Outline each blood parasite and name the species.
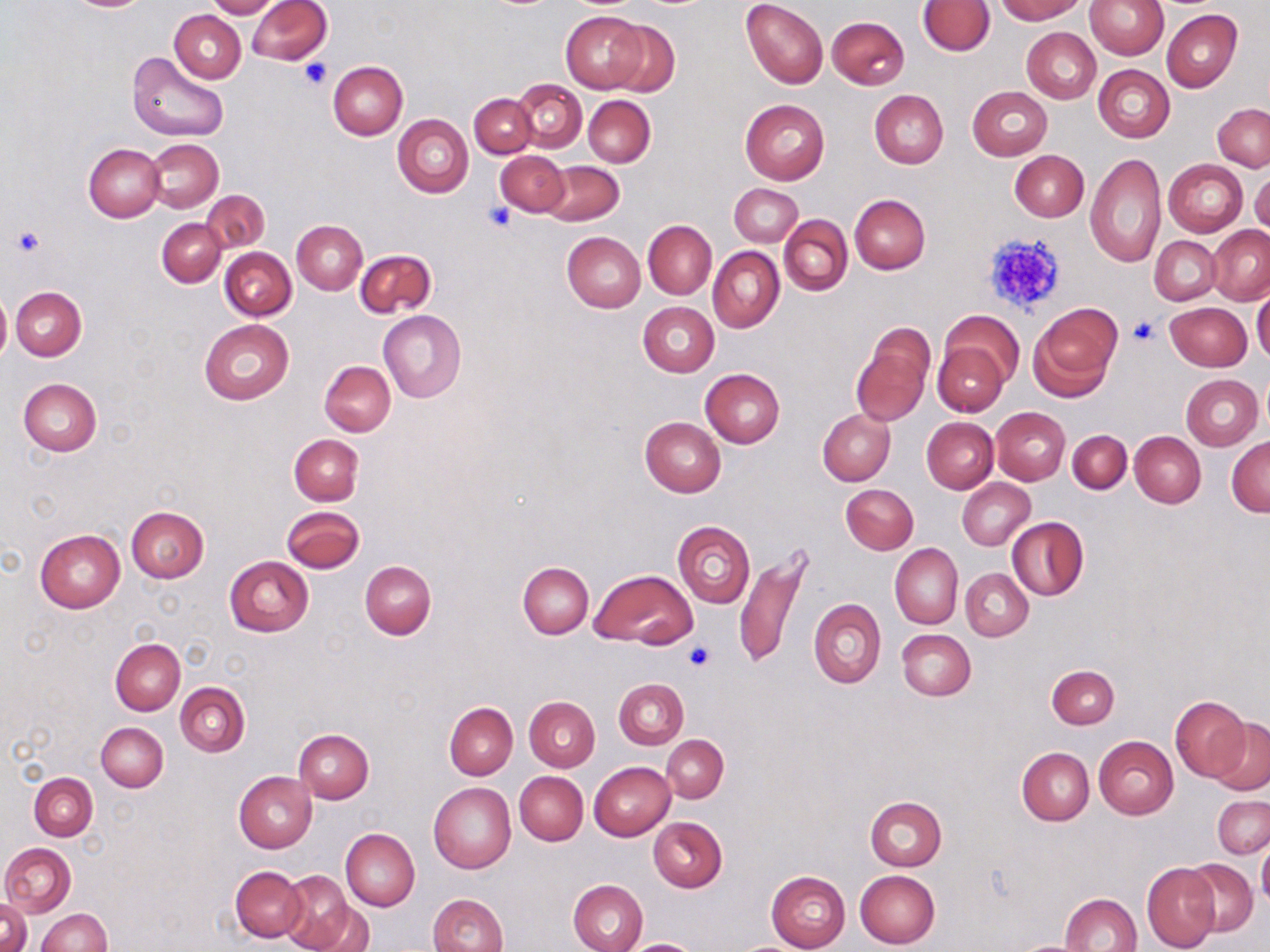

No blood parasites seen.

Summary:
  - Coordinate format: approximate bounding boxes as [x1, y1, x2, y2] in pixels
  - Uninfected red blood cell locations: [207, 0, 280, 18], [247, 0, 331, 64], [741, 0, 828, 88], [995, 0, 1085, 22], [1084, 0, 1168, 59], [919, 1, 994, 55], [170, 9, 246, 83], [1162, 9, 1241, 91], [562, 11, 648, 93], [827, 16, 909, 89], [603, 20, 681, 96], [1021, 27, 1099, 102], [126, 50, 229, 142], [329, 61, 408, 140], [1093, 64, 1175, 142], [513, 80, 587, 151], [967, 86, 1052, 160], [870, 90, 948, 169], [470, 93, 537, 158], [584, 96, 655, 166], [739, 99, 829, 185], [1213, 104, 1269, 172], [393, 114, 473, 197], [145, 138, 224, 213], [84, 143, 164, 222], [1010, 150, 1089, 222], [496, 151, 569, 216], [1083, 153, 1164, 269], [1164, 159, 1248, 237], [540, 161, 623, 226], [1250, 168, 1270, 237], [729, 183, 804, 246], [201, 190, 269, 253], [850, 194, 930, 274], [779, 215, 852, 296], [157, 218, 226, 287], [643, 220, 716, 298], [292, 221, 367, 294], [1207, 225, 1270, 304], [563, 232, 646, 312], [293, 234, 435, 307], [1150, 236, 1221, 306], [708, 246, 784, 333], [221, 248, 295, 320], [356, 249, 436, 317], [11, 286, 86, 361], [1252, 290, 1270, 364], [0, 291, 10, 368], [637, 302, 718, 376], [1166, 302, 1251, 371], [1028, 304, 1120, 398], [378, 309, 466, 403], [937, 311, 1021, 393], [199, 320, 294, 404], [853, 325, 934, 426], [932, 328, 1009, 491], [934, 341, 1010, 417], [320, 361, 395, 436], [1259, 368, 1270, 436], [700, 369, 784, 448], [1181, 374, 1264, 449], [18, 378, 101, 456], [992, 408, 1070, 485], [817, 410, 895, 485], [640, 416, 727, 497], [922, 417, 998, 493], [1068, 430, 1131, 494], [1130, 431, 1206, 507], [289, 434, 363, 506], [1226, 437, 1270, 516], [957, 478, 1034, 550], [841, 484, 918, 554], [126, 506, 209, 582], [282, 507, 364, 573], [1007, 517, 1090, 601], [672, 521, 755, 608], [35, 528, 125, 613], [890, 543, 963, 629], [733, 550, 812, 670], [224, 556, 314, 637], [361, 561, 436, 638], [518, 562, 593, 638], [960, 568, 1033, 641], [589, 569, 697, 647], [810, 598, 886, 688], [897, 628, 976, 700], [110, 638, 185, 715], [1046, 664, 1119, 728], [614, 677, 688, 749], [175, 683, 249, 756], [1171, 696, 1249, 779], [525, 697, 600, 771], [445, 702, 518, 779], [1207, 718, 1269, 794], [96, 722, 168, 791], [294, 728, 374, 803], [661, 734, 728, 802], [1093, 736, 1178, 819], [1017, 747, 1094, 825], [589, 761, 675, 841], [515, 771, 588, 845], [234, 772, 315, 853], [29, 773, 98, 840], [429, 783, 516, 874], [865, 796, 946, 871], [1212, 796, 1270, 859], [649, 817, 727, 892], [340, 828, 419, 911], [1258, 838, 1270, 910], [1, 842, 75, 915], [1181, 859, 1258, 937], [1142, 864, 1219, 951], [231, 865, 307, 943], [854, 869, 940, 948], [279, 870, 360, 952], [766, 870, 851, 952], [568, 879, 648, 952], [1059, 892, 1141, 952], [428, 893, 508, 952], [0, 899, 31, 952], [308, 903, 372, 952], [37, 909, 110, 952], [1011, 938, 1102, 952], [624, 939, 705, 951]
  - Platelet locations: [298, 59, 331, 90], [484, 203, 517, 231], [11, 225, 46, 256], [980, 231, 1068, 318], [1129, 317, 1160, 345], [683, 642, 716, 672]
  - Slide-level diagnosis: negative for blood parasites
  - Field of view: single
  - Stain: May-Grünwald-Giemsa
  - Magnification: 1000x
  - Preparation: thin blood smear
  - Modality: optical microscopy
  - Image size: 1270×952 pixels